State the preparation type.
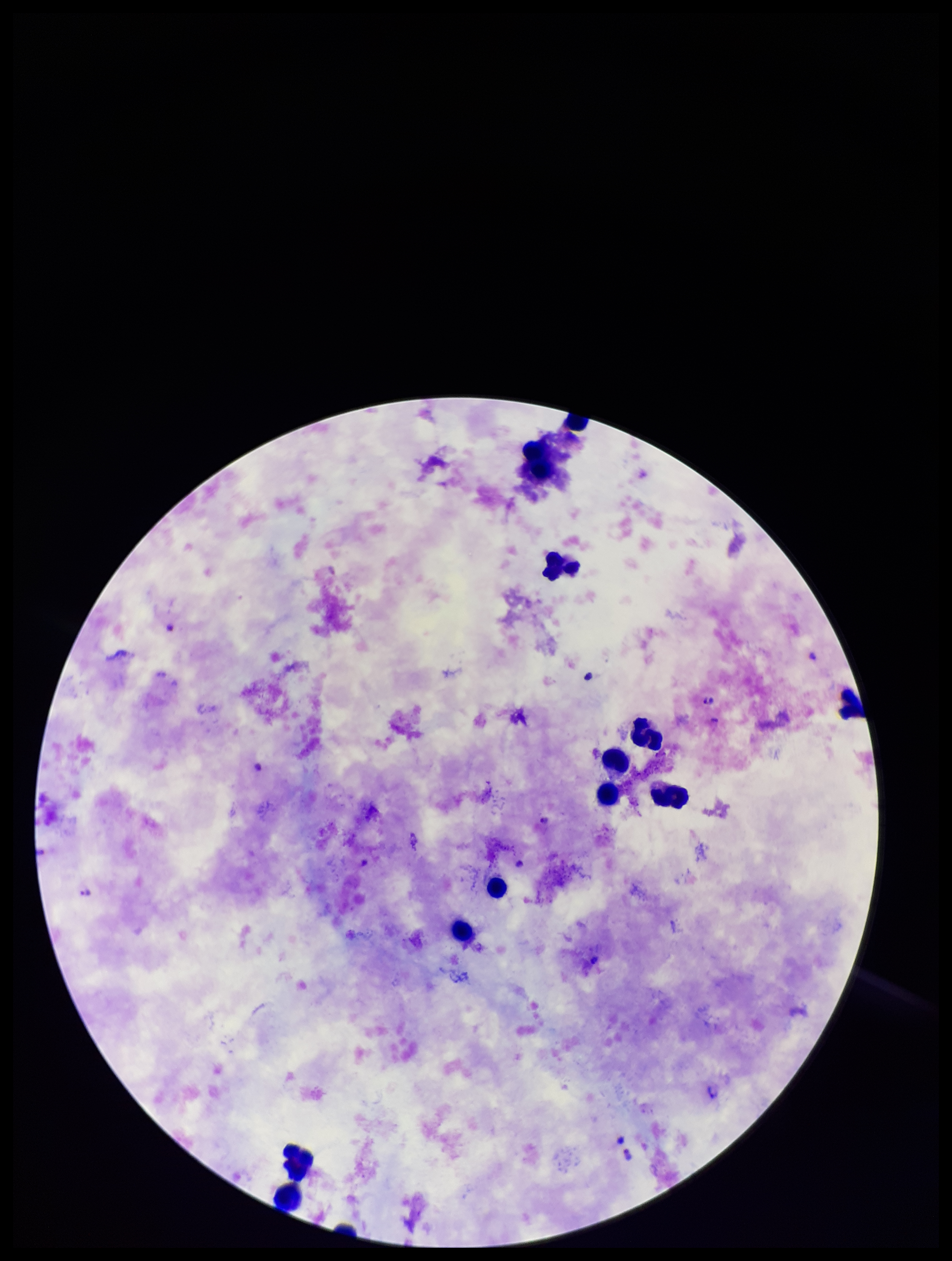

A thick smear.

Summary:
  - Field of view: single
  - Species reported for this patient: Plasmodium falciparum
  - Parasite count: 4
  - Plasmodium parasites: detected
  - Image size: 952×1261 pixels
  - Patient malaria status: infected
  - Leukocyte count: 11
  - Capture: smartphone photograph through the microscope eyepiece
  - Stain: Giemsa